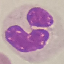

{
  "result": "no malaria parasites seen",
  "stain": "Giemsa",
  "preparation": "thin smear",
  "image_type": "automatically extracted cell patch, resized to 64 × 64 pixels",
  "capture": "smartphone through the microscope eyepiece"
}